Outline every trophozoite.
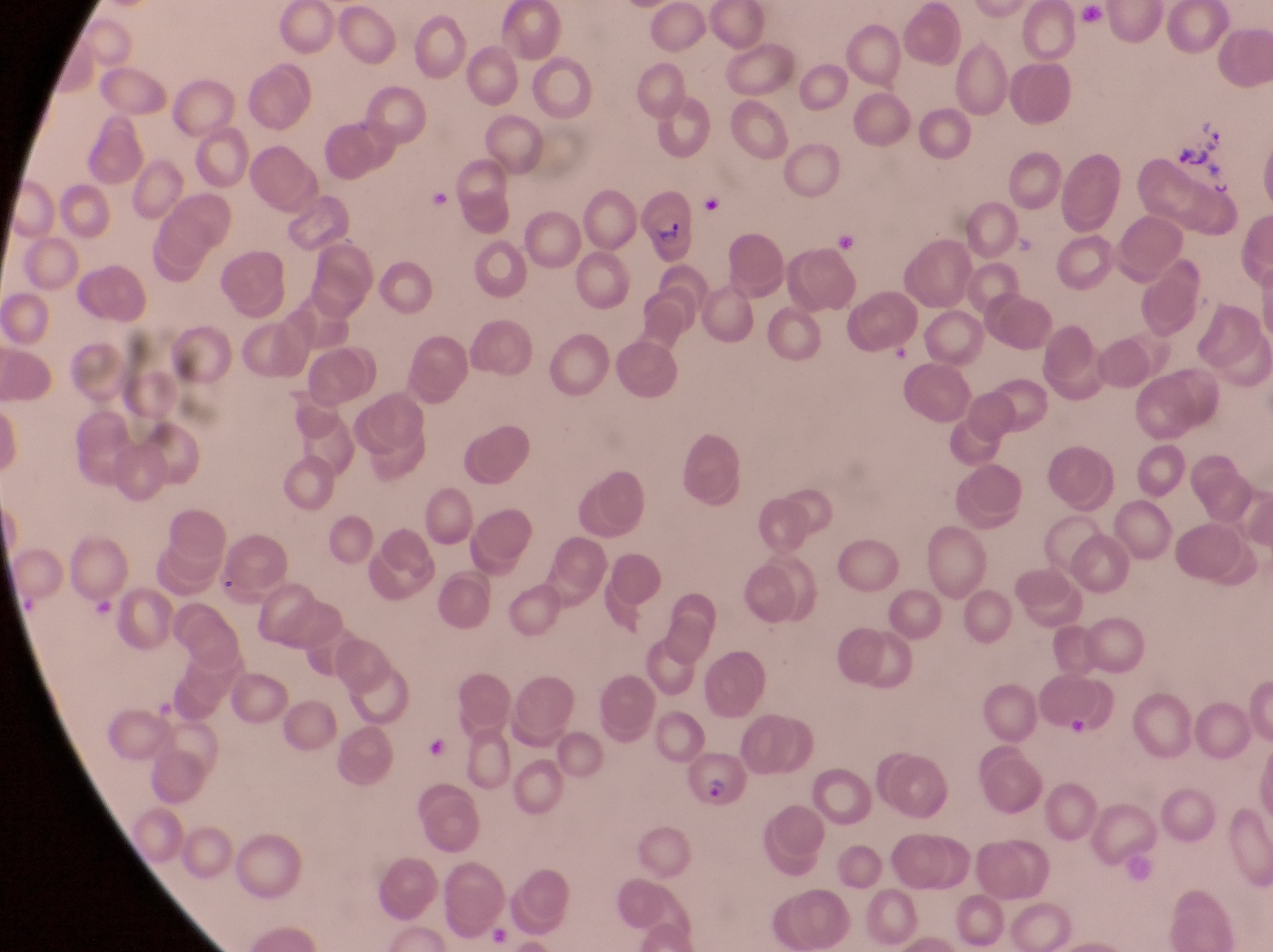

Approximate bounding boxes as left top right bottom in pixels.
Trophozoites: 1199 125 1227 155; 1208 174 1240 199.

field of view = single
preparation = thin blood smear
parasitised red blood cell locations = approximate bounding boxes as left top right bottom in pixels: 641 180 701 267; 684 755 751 805
country = Uganda
capture = smartphone photograph through the eyepiece of an Olympus CX-23 microscope
magnification = 1000x
image size = 1273×952 pixels